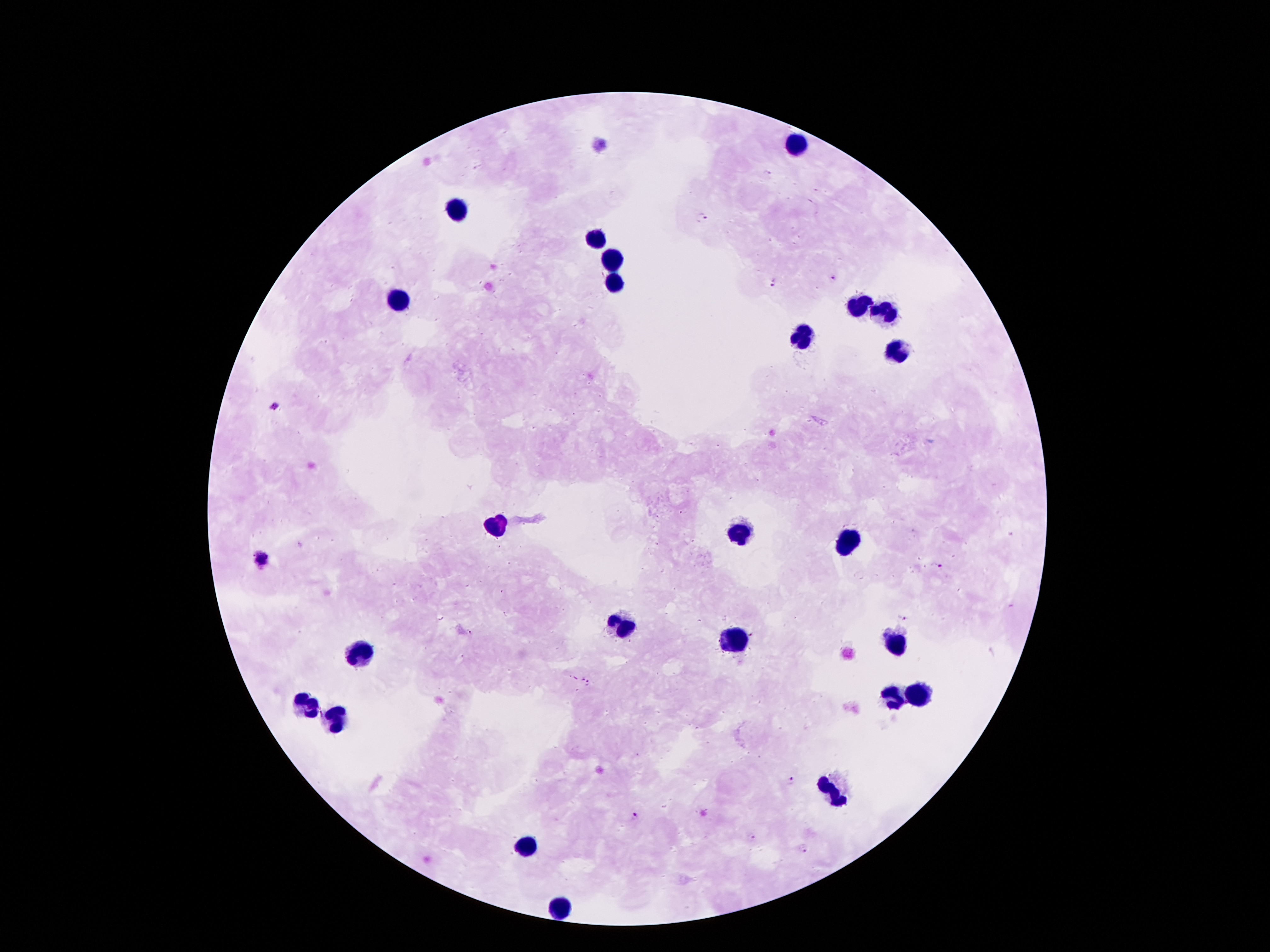
Approximate object centers, in pixels from the top-left corner.
Summary:
  - Leukocyte locations: (x=794, y=145), (x=456, y=208), (x=593, y=238), (x=614, y=257), (x=615, y=283), (x=399, y=300), (x=857, y=309), (x=887, y=313), (x=803, y=337), (x=900, y=354), (x=497, y=524), (x=743, y=533), (x=842, y=541), (x=623, y=627), (x=739, y=639), (x=894, y=643), (x=361, y=654), (x=921, y=694), (x=896, y=698), (x=308, y=708), (x=336, y=721), (x=835, y=792), (x=525, y=847), (x=555, y=906)
  - Malaria parasite locations: (x=702, y=219), (x=833, y=277), (x=772, y=282), (x=275, y=407), (x=259, y=559), (x=937, y=566), (x=904, y=614), (x=586, y=681), (x=791, y=781), (x=635, y=817), (x=753, y=837), (x=803, y=850)
  - Image size: 1270×952 pixels
  - Capture: smartphone camera through the microscope eyepiece
  - Preparation: thick blood smear
  - Magnification: 100x
  - Patient malaria status: positive for Plasmodium falciparum
  - Field of view: one from this slide
  - Stain: Giemsa